Report the malaria status of this cell.
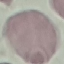

Uninfected.

Thin blood film. Giemsa stain. Automatically extracted cell patch, resized to 64 × 64 pixels. Photographed with a smartphone camera at the microscope eyepiece.